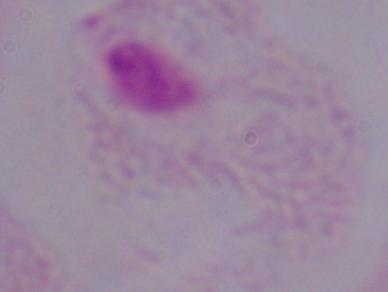
1000x magnification. A trichomonad is seen. Micrograph.